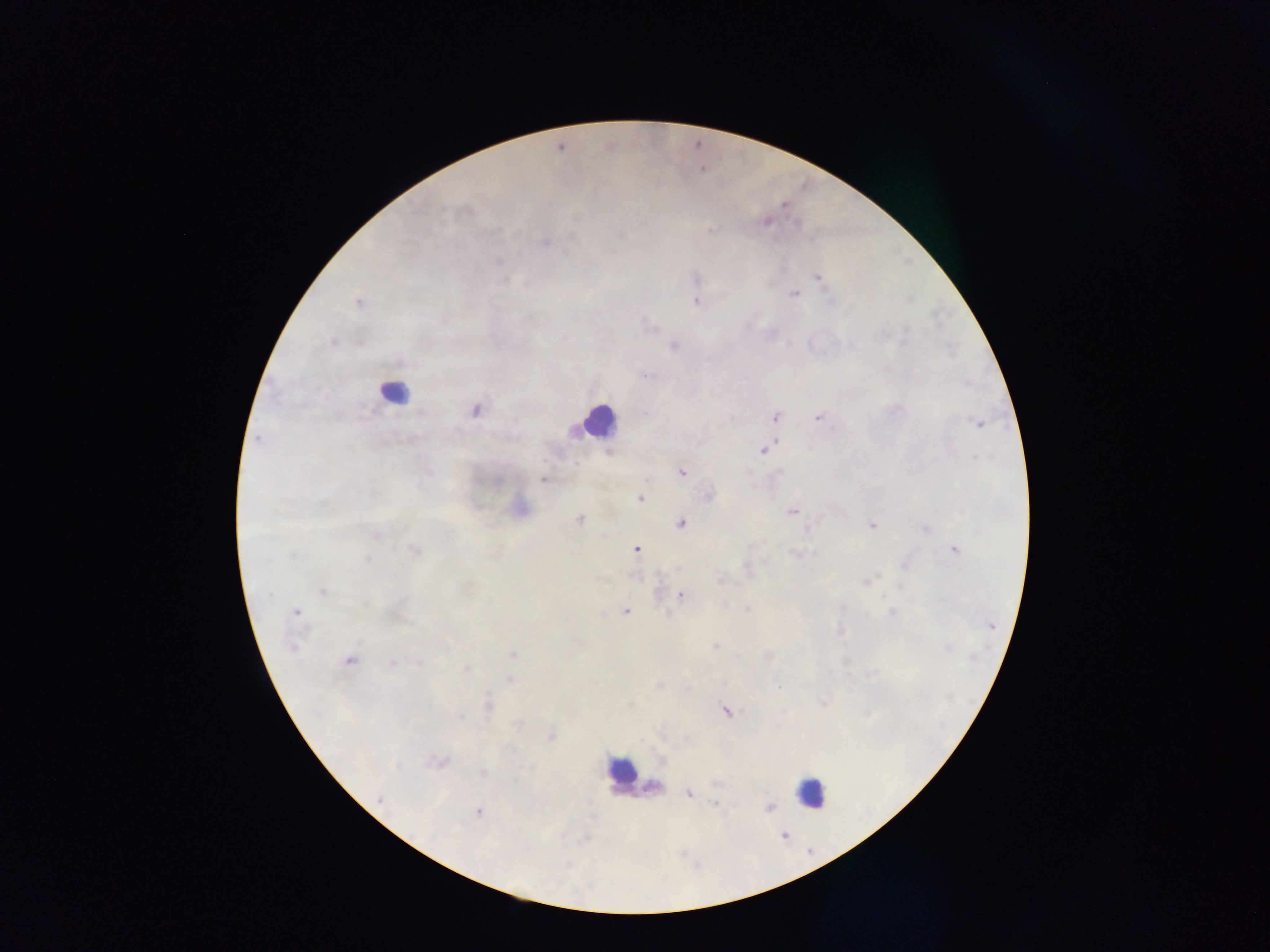
country: Ghana
image_size: 1270×952 pixels
preparation: thick blood film
malaria_parasite_locations: 'approximate centers as (x, y) in pixels: (781, 207), (461, 213), (765, 219), (795, 223), (711, 229), (492, 232), (622, 234), (545, 243), (498, 259), (695, 276), (816, 278), (505, 280), (504, 281), (794, 294), (696, 302), (357, 304), (650, 326), (908, 330), (334, 342), (673, 345), (646, 376), (475, 409), (774, 417), (816, 417), (977, 425), (255, 439), (768, 448), (763, 450), (976, 457), (426, 470), (680, 471), (778, 472), (543, 479), (707, 494), (639, 499), (792, 513), (579, 519), (682, 526), (870, 527), (806, 530), (379, 536), (637, 549), (955, 549), (415, 550), (794, 552), (290, 556), (367, 559), (747, 568), (879, 575), (865, 582), (322, 593), (679, 595), (402, 602), (746, 609), (294, 612), (893, 612), (626, 613), (668, 615), (716, 646), (290, 647), (768, 654), (514, 655), (349, 661), (417, 662), (392, 663), (466, 670), (510, 680), (660, 684), (778, 685), (631, 704), (822, 704), (486, 705), (726, 712), (462, 717), (518, 724), (552, 736), (438, 763), (430, 765), (399, 767), (482, 773), (716, 785), (654, 788), (689, 794), (716, 805), (770, 805), (478, 813), (568, 865)'
leukocyte_locations: 'approximate centers as (x, y) in pixels: (394, 393), (594, 424), (616, 771), (814, 793)'
capture: mobile-phone photograph through a microscope
field_of_view: single